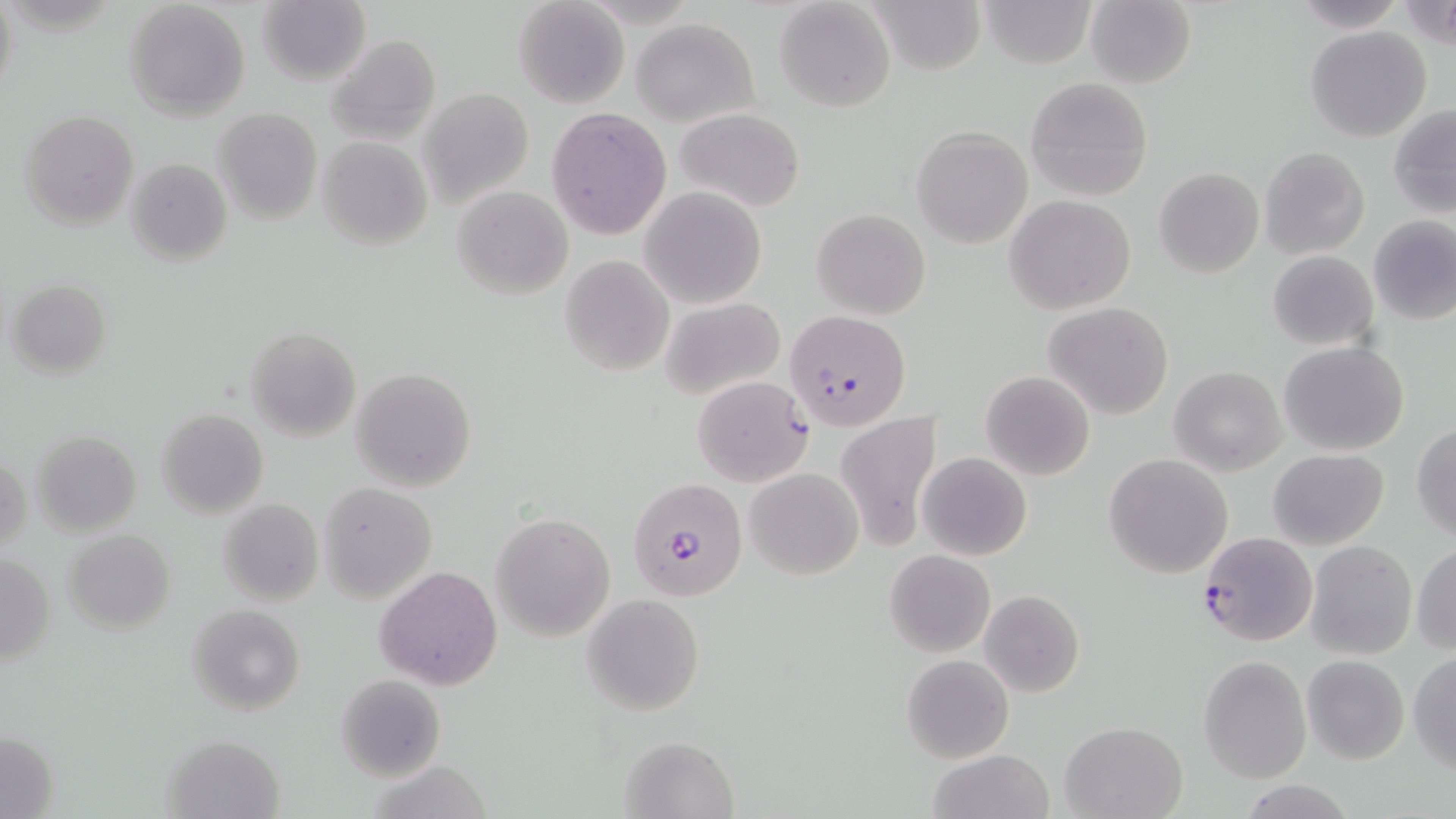

{
  "slide_level_diagnosis": "Plasmodium falciparum",
  "stain": "May-Grünwald-Giemsa",
  "uninfected_red_blood_cell_locations": "approximate bounding boxes as named x1/y1/x2/y2 corners in pixels: (x1=774, y1=0, x2=896, y2=113), (x1=865, y1=0, x2=988, y2=75), (x1=978, y1=0, x2=1099, y2=69), (x1=1287, y1=0, x2=1408, y2=32), (x1=125, y1=1, x2=251, y2=120), (x1=514, y1=1, x2=629, y2=110), (x1=1085, y1=1, x2=1197, y2=89), (x1=257, y1=2, x2=370, y2=86), (x1=631, y1=18, x2=757, y2=126), (x1=1305, y1=26, x2=1431, y2=142), (x1=325, y1=34, x2=441, y2=145), (x1=1024, y1=77, x2=1154, y2=201), (x1=420, y1=88, x2=536, y2=206), (x1=1389, y1=104, x2=1456, y2=217), (x1=547, y1=106, x2=672, y2=241), (x1=675, y1=107, x2=805, y2=211), (x1=213, y1=109, x2=322, y2=225), (x1=21, y1=110, x2=140, y2=230), (x1=912, y1=128, x2=1032, y2=248), (x1=317, y1=137, x2=433, y2=251), (x1=1260, y1=146, x2=1369, y2=260), (x1=124, y1=157, x2=232, y2=267), (x1=1154, y1=167, x2=1264, y2=278), (x1=451, y1=185, x2=575, y2=300), (x1=639, y1=186, x2=767, y2=310), (x1=1005, y1=195, x2=1136, y2=315), (x1=811, y1=208, x2=931, y2=318), (x1=1369, y1=217, x2=1456, y2=325), (x1=1266, y1=251, x2=1378, y2=350), (x1=559, y1=256, x2=674, y2=377), (x1=6, y1=278, x2=112, y2=378), (x1=660, y1=297, x2=785, y2=398), (x1=1045, y1=301, x2=1172, y2=420), (x1=246, y1=326, x2=360, y2=442), (x1=1278, y1=341, x2=1410, y2=456), (x1=1169, y1=365, x2=1286, y2=474), (x1=350, y1=366, x2=478, y2=492), (x1=981, y1=371, x2=1095, y2=480), (x1=691, y1=375, x2=811, y2=487), (x1=155, y1=408, x2=268, y2=518), (x1=833, y1=410, x2=940, y2=550), (x1=1412, y1=424, x2=1456, y2=543), (x1=30, y1=430, x2=143, y2=536), (x1=1269, y1=449, x2=1389, y2=549), (x1=1, y1=451, x2=30, y2=558), (x1=918, y1=452, x2=1032, y2=561), (x1=1104, y1=454, x2=1234, y2=579), (x1=745, y1=466, x2=863, y2=580), (x1=320, y1=482, x2=439, y2=603), (x1=217, y1=499, x2=324, y2=607), (x1=491, y1=512, x2=615, y2=641), (x1=63, y1=528, x2=177, y2=634), (x1=1305, y1=541, x2=1416, y2=659), (x1=1411, y1=541, x2=1456, y2=657), (x1=884, y1=549, x2=995, y2=656), (x1=1, y1=554, x2=56, y2=668), (x1=374, y1=565, x2=502, y2=690), (x1=978, y1=590, x2=1086, y2=698), (x1=581, y1=593, x2=706, y2=715), (x1=187, y1=604, x2=305, y2=715), (x1=1408, y1=651, x2=1456, y2=773), (x1=902, y1=654, x2=1013, y2=763), (x1=1302, y1=654, x2=1409, y2=764), (x1=1199, y1=655, x2=1312, y2=783), (x1=335, y1=673, x2=445, y2=782), (x1=1060, y1=721, x2=1187, y2=819), (x1=2, y1=729, x2=57, y2=819), (x1=161, y1=733, x2=286, y2=819), (x1=620, y1=733, x2=742, y2=819), (x1=925, y1=749, x2=1055, y2=819), (x1=1238, y1=781, x2=1359, y2=818)",
  "modality": "light microscopy",
  "plasmodium_falciparum_infected_red_blood_cell_locations": "approximate bounding boxes as named x1/y1/x2/y2 corners in pixels: (x1=788, y1=310, x2=910, y2=429), (x1=625, y1=477, x2=748, y2=602), (x1=1198, y1=531, x2=1318, y2=647)",
  "magnification": "1000x",
  "field_of_view": "single",
  "preparation": "thin blood film",
  "image_size": "1456×819 pixels"
}